Outline each blood parasite and name the species.
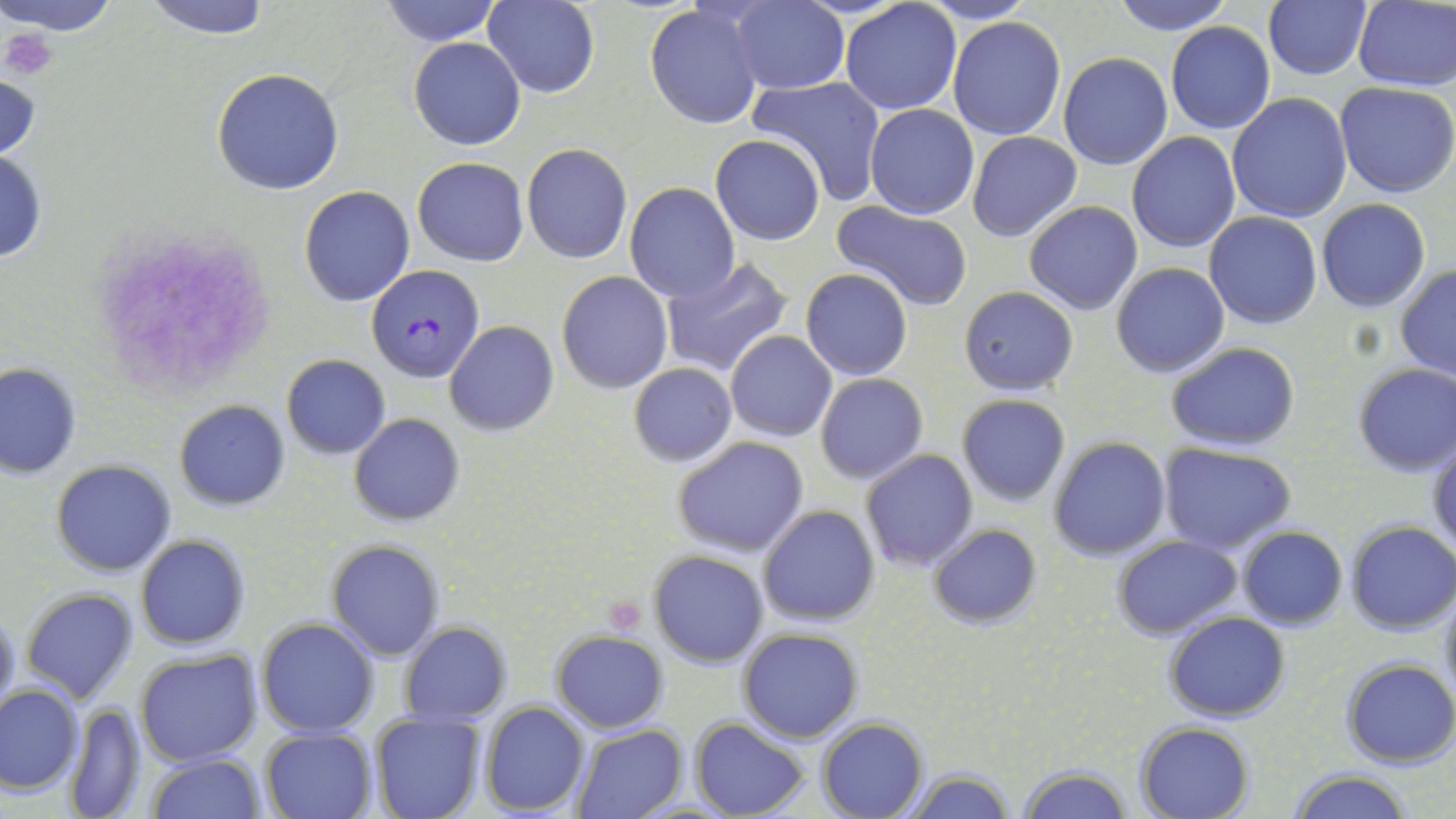
Approximate bounding boxes as (x1, y1, x2, y2) in pixels.
Plasmodium falciparum-infected red blood cells: (368, 263, 483, 381).
No Plasmodium ovale, Plasmodium malariae, Plasmodium vivax, Babesia divergens, or Trypanosoma brucei observed.

Platelet locations: (4, 27, 58, 78), (100, 235, 273, 396), (604, 597, 647, 634). Uninfected red blood cell locations: (1, 0, 118, 36), (142, 0, 275, 39), (379, 0, 500, 47), (483, 0, 598, 97), (840, 0, 961, 116), (914, 0, 1040, 25), (1110, 0, 1235, 35), (729, 1, 848, 94), (1263, 1, 1371, 80), (1351, 1, 1456, 89), (644, 3, 764, 129), (948, 16, 1066, 140), (1165, 22, 1275, 134), (410, 38, 526, 148), (1058, 53, 1173, 170), (212, 68, 344, 195), (0, 72, 42, 162), (749, 75, 888, 204), (1334, 82, 1456, 199), (1226, 93, 1354, 224), (864, 103, 979, 219), (967, 130, 1082, 242), (1126, 131, 1241, 253), (711, 134, 825, 245), (522, 143, 632, 264), (0, 150, 47, 264), (413, 157, 528, 266), (625, 183, 741, 301), (299, 185, 415, 307), (1315, 199, 1430, 312), (1024, 200, 1142, 316), (831, 202, 975, 311), (1204, 211, 1322, 330), (660, 257, 793, 376), (1111, 263, 1229, 378), (1395, 265, 1456, 380), (802, 268, 913, 380), (557, 271, 672, 393), (958, 286, 1079, 395), (444, 320, 559, 436), (725, 330, 836, 442), (1164, 342, 1300, 451), (282, 355, 390, 458), (1, 363, 80, 479), (628, 363, 738, 467), (1352, 363, 1456, 477), (815, 373, 927, 484), (956, 393, 1071, 507), (174, 400, 290, 511), (350, 414, 464, 525), (672, 436, 809, 557), (1048, 436, 1172, 561), (1427, 437, 1456, 555), (1158, 443, 1295, 553), (861, 449, 977, 570), (49, 458, 177, 578), (758, 504, 881, 626), (1346, 520, 1456, 634), (927, 523, 1042, 630), (1237, 527, 1348, 629), (134, 533, 250, 651), (1112, 535, 1243, 638), (326, 539, 446, 660), (648, 549, 769, 668), (21, 588, 138, 705), (1437, 588, 1456, 705), (0, 608, 21, 718), (1166, 611, 1290, 721), (257, 618, 380, 736), (399, 623, 511, 727), (737, 627, 863, 743), (551, 630, 667, 733), (135, 649, 263, 767), (1340, 659, 1455, 769), (0, 683, 83, 795), (480, 701, 590, 817), (63, 703, 150, 818), (368, 710, 485, 819), (691, 717, 810, 818), (816, 717, 928, 819), (1136, 721, 1254, 818), (572, 725, 689, 818), (259, 727, 375, 818), (145, 754, 266, 819), (1016, 763, 1131, 819), (900, 768, 1017, 818), (1289, 769, 1415, 819). Slide-level diagnosis: Plasmodium falciparum. Captured at 1000x magnification. Optical microscopy. Image is 1456×819 pixels. One field of a larger specimen. Thin blood film. May-Grünwald-Giemsa-stained preparation.